Give the extent of all Plasmodium ovale-infected red blood cells.
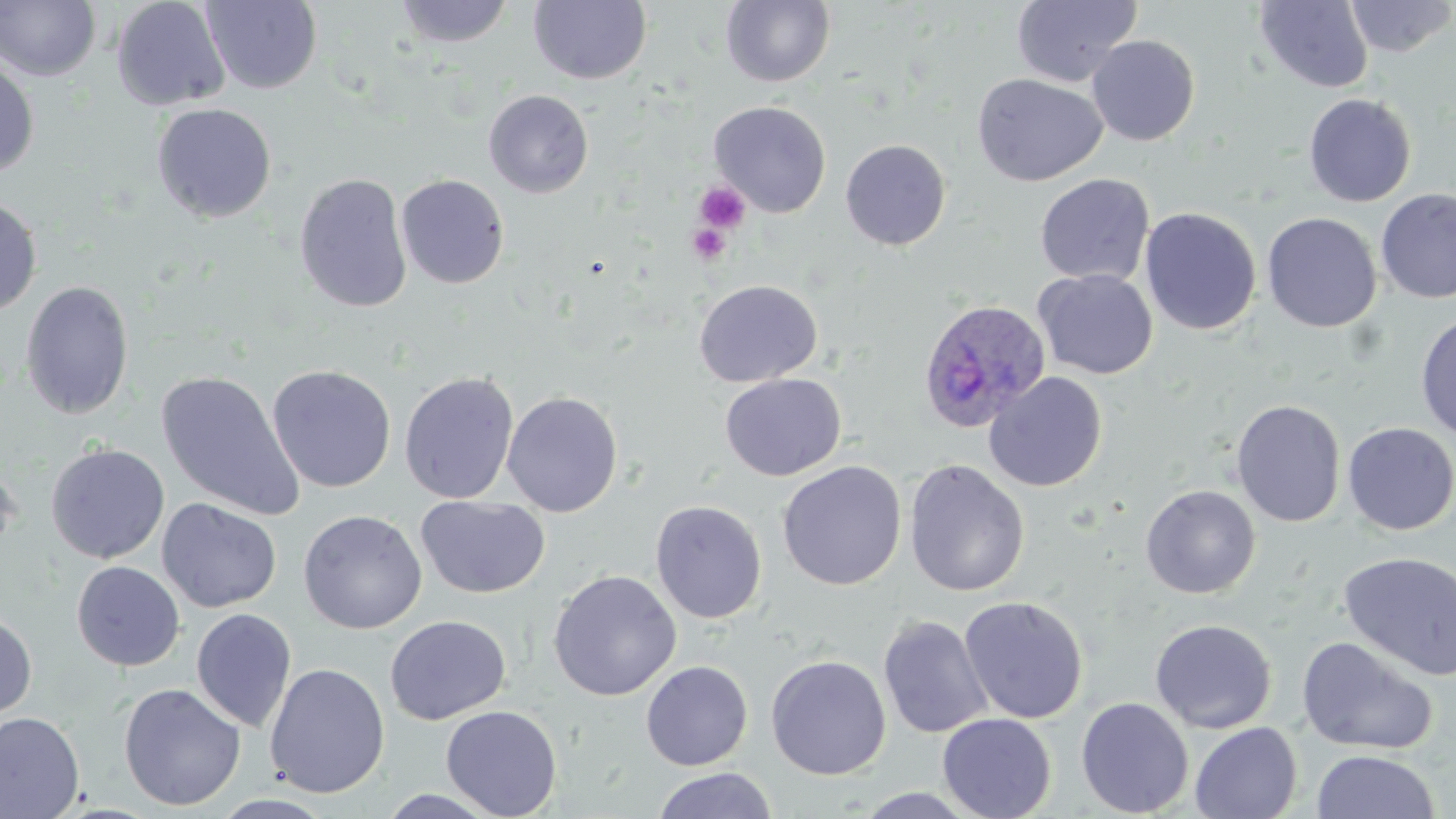

Approximate bounding boxes as named x1/y1/x2/y2 corners in pixels.
Plasmodium ovale-infected red blood cells: (x1=917, y1=298, x2=1052, y2=434).

slide-level diagnosis = Plasmodium ovale
uninfected red blood cell locations = approximate bounding boxes as named x1/y1/x2/y2 corners in pixels: (x1=110, y1=0, x2=231, y2=111), (x1=394, y1=0, x2=514, y2=48), (x1=720, y1=0, x2=836, y2=88), (x1=1012, y1=0, x2=1142, y2=88), (x1=1346, y1=0, x2=1456, y2=58), (x1=0, y1=1, x2=101, y2=82), (x1=201, y1=1, x2=323, y2=94), (x1=529, y1=1, x2=652, y2=85), (x1=1255, y1=1, x2=1373, y2=92), (x1=1086, y1=35, x2=1200, y2=146), (x1=0, y1=58, x2=40, y2=180), (x1=972, y1=73, x2=1107, y2=187), (x1=483, y1=89, x2=594, y2=198), (x1=1303, y1=93, x2=1417, y2=207), (x1=708, y1=101, x2=832, y2=217), (x1=152, y1=103, x2=277, y2=223), (x1=840, y1=139, x2=951, y2=251), (x1=294, y1=173, x2=412, y2=313), (x1=1035, y1=173, x2=1155, y2=287), (x1=395, y1=174, x2=510, y2=289), (x1=1376, y1=189, x2=1456, y2=304), (x1=0, y1=195, x2=42, y2=317), (x1=1139, y1=207, x2=1262, y2=336), (x1=1262, y1=212, x2=1382, y2=333), (x1=1034, y1=269, x2=1158, y2=380), (x1=693, y1=279, x2=823, y2=387), (x1=20, y1=280, x2=134, y2=420), (x1=1415, y1=311, x2=1456, y2=442), (x1=267, y1=365, x2=396, y2=492), (x1=157, y1=371, x2=305, y2=521), (x1=399, y1=371, x2=519, y2=504), (x1=983, y1=371, x2=1108, y2=493), (x1=719, y1=373, x2=846, y2=481), (x1=502, y1=391, x2=623, y2=517), (x1=1231, y1=399, x2=1346, y2=527), (x1=1342, y1=422, x2=1456, y2=535), (x1=46, y1=443, x2=169, y2=563), (x1=0, y1=457, x2=22, y2=562), (x1=903, y1=459, x2=1030, y2=597), (x1=777, y1=461, x2=907, y2=590), (x1=1140, y1=485, x2=1261, y2=599), (x1=416, y1=495, x2=551, y2=599), (x1=157, y1=498, x2=282, y2=612), (x1=649, y1=500, x2=767, y2=624), (x1=298, y1=510, x2=427, y2=634), (x1=1338, y1=551, x2=1456, y2=680), (x1=72, y1=561, x2=185, y2=671), (x1=547, y1=569, x2=682, y2=701), (x1=959, y1=596, x2=1088, y2=724), (x1=191, y1=608, x2=297, y2=732), (x1=0, y1=609, x2=37, y2=723), (x1=878, y1=614, x2=993, y2=739), (x1=385, y1=615, x2=511, y2=725), (x1=1149, y1=619, x2=1277, y2=734), (x1=1296, y1=636, x2=1440, y2=755), (x1=766, y1=654, x2=891, y2=780), (x1=641, y1=660, x2=753, y2=771), (x1=264, y1=663, x2=390, y2=798), (x1=118, y1=682, x2=246, y2=811), (x1=1076, y1=697, x2=1194, y2=817), (x1=440, y1=705, x2=562, y2=818), (x1=0, y1=711, x2=85, y2=819), (x1=937, y1=713, x2=1057, y2=819), (x1=1190, y1=721, x2=1302, y2=819), (x1=1310, y1=750, x2=1441, y2=819), (x1=652, y1=767, x2=779, y2=819), (x1=853, y1=788, x2=982, y2=818), (x1=375, y1=789, x2=505, y2=818)
platelet locations = approximate bounding boxes as named x1/y1/x2/y2 corners in pixels: (x1=694, y1=182, x2=751, y2=234), (x1=686, y1=223, x2=732, y2=266)
modality = optical microscopy
stain = May-Grünwald-Giemsa
field of view = single
image size = 1456×819 pixels
magnification = 1000x
preparation = thin blood film